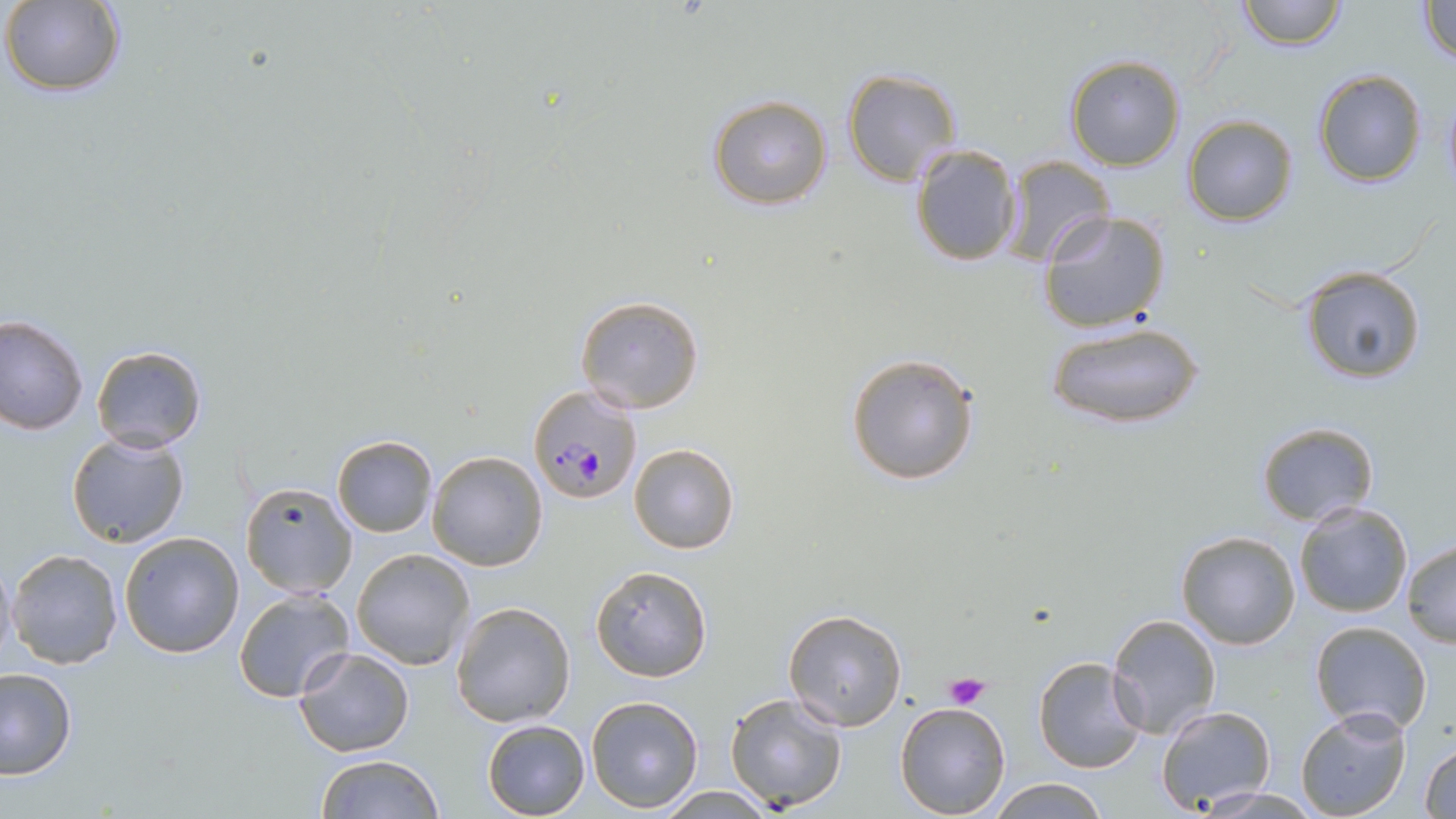
Summary:
  - Coordinate format: approximate bounding boxes as [x1, y1, x2, y2] in pixels
  - Plasmodium falciparum-infected red blood cell locations: [527, 385, 641, 505]
  - Platelet locations: [942, 673, 991, 709]
  - Uninfected red blood cell locations: [1236, 0, 1347, 50], [1414, 0, 1456, 66], [3, 2, 126, 97], [1064, 56, 1185, 171], [841, 68, 961, 184], [1311, 69, 1428, 187], [1441, 85, 1456, 193], [708, 94, 833, 209], [1182, 114, 1299, 227], [908, 143, 1021, 268], [1003, 155, 1115, 269], [1038, 209, 1171, 333], [1299, 267, 1427, 384], [575, 295, 705, 414], [0, 314, 89, 434], [1049, 321, 1204, 430], [91, 343, 208, 452], [845, 351, 982, 486], [1256, 421, 1378, 525], [66, 432, 193, 548], [332, 435, 437, 537], [628, 442, 740, 554], [427, 451, 548, 571], [239, 482, 357, 598], [1294, 502, 1414, 619], [1175, 530, 1302, 651], [118, 531, 245, 658], [1401, 540, 1456, 648], [7, 547, 123, 668], [350, 548, 474, 670], [1, 549, 16, 669], [590, 565, 712, 681], [233, 589, 355, 703], [451, 599, 576, 727], [784, 609, 908, 732], [1104, 612, 1220, 740], [1309, 620, 1435, 734], [295, 647, 414, 757], [1031, 655, 1147, 774], [0, 667, 76, 779], [725, 692, 848, 811], [586, 694, 705, 811], [895, 701, 1011, 819], [1154, 705, 1276, 812], [1295, 707, 1413, 819], [481, 718, 590, 818], [1419, 742, 1456, 819], [315, 753, 442, 819], [984, 777, 1109, 817], [655, 786, 775, 818], [1192, 786, 1322, 818]
  - Slide-level diagnosis: Plasmodium falciparum
  - Modality: light microscopy
  - Field of view: single
  - Magnification: 1000x
  - Image size: 1456×819 pixels
  - Preparation: thin blood smear
  - Stain: May-Grünwald-Giemsa